Locate every Plasmodium vivax-infected red blood cell.
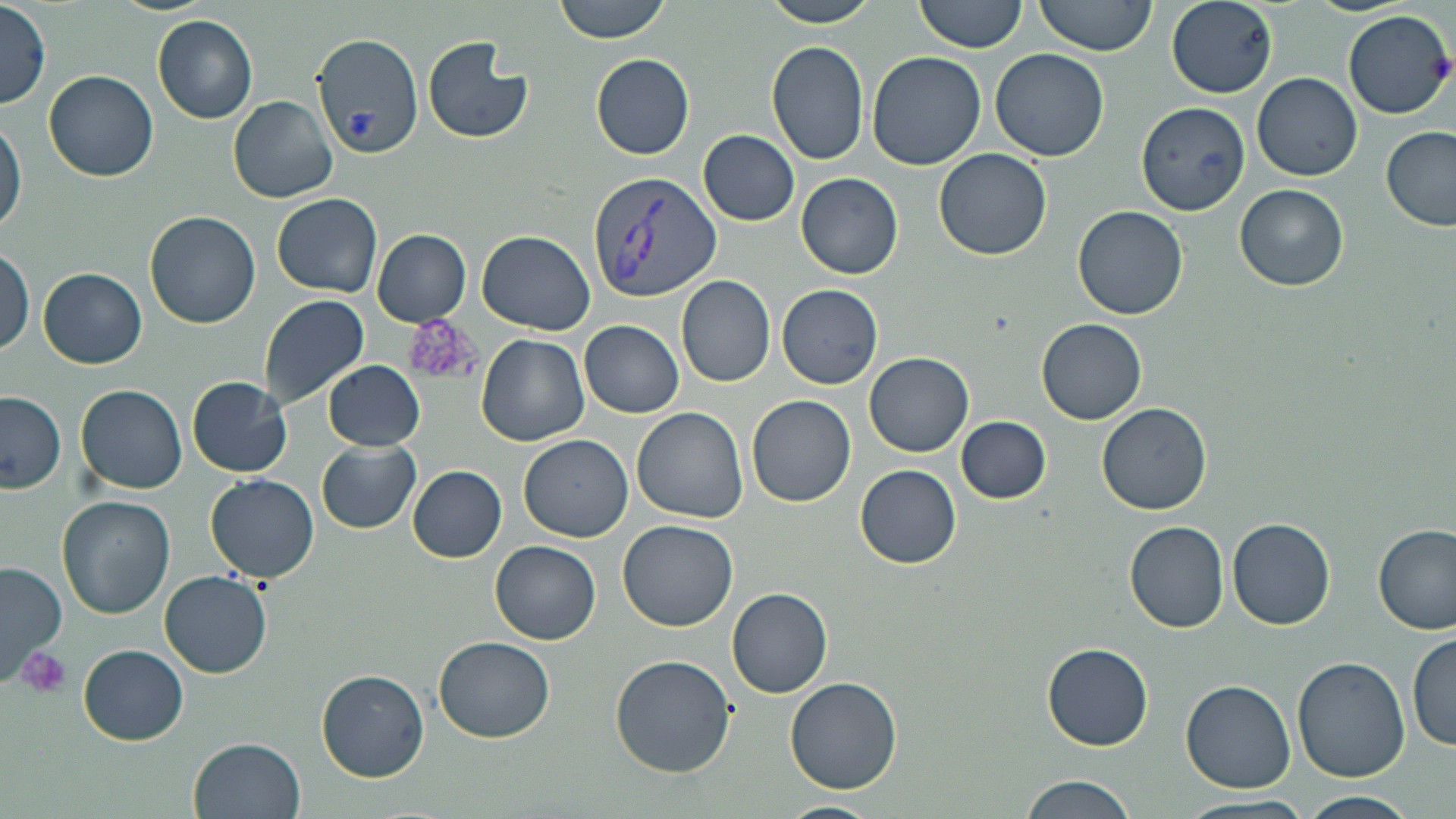

Approximate bounding boxes as [x1, y1, x2, y2] in pixels.
Plasmodium vivax-infected red blood cells: [588, 171, 720, 301].

{
  "slide_level_diagnosis": "Plasmodium vivax",
  "modality": "optical microscopy",
  "image_size": "1456×819 pixels",
  "stain": "May-Grünwald-Giemsa",
  "preparation": "thin blood smear",
  "uninfected_red_blood_cell_locations": "approximate bounding boxes as [x1, y1, x2, y2] in pixels: [552, 0, 672, 43], [759, 0, 881, 26], [914, 0, 1028, 53], [1035, 0, 1157, 55], [1166, 1, 1278, 98], [0, 2, 49, 109], [1343, 9, 1454, 120], [151, 15, 258, 124], [312, 31, 423, 158], [423, 35, 534, 144], [765, 40, 870, 166], [990, 49, 1110, 162], [866, 52, 988, 171], [590, 53, 694, 159], [44, 69, 157, 182], [1251, 72, 1361, 181], [227, 95, 337, 204], [1136, 102, 1252, 216], [1, 116, 28, 235], [1380, 126, 1456, 232], [698, 129, 800, 226], [933, 148, 1053, 260], [795, 173, 903, 279], [1233, 183, 1350, 291], [272, 193, 383, 297], [1071, 205, 1188, 321], [144, 210, 262, 328], [372, 229, 471, 327], [476, 230, 595, 335], [0, 247, 34, 355], [38, 267, 146, 369], [676, 275, 775, 387], [777, 284, 884, 389], [258, 295, 370, 410], [1036, 318, 1149, 424], [578, 321, 683, 417], [476, 334, 589, 446], [863, 352, 974, 458], [322, 361, 425, 450], [186, 376, 292, 478], [75, 385, 188, 495], [0, 392, 65, 492], [746, 394, 856, 507], [1095, 402, 1214, 515], [631, 407, 748, 524], [957, 417, 1052, 503], [519, 435, 633, 541], [316, 440, 421, 534], [320, 457, 502, 553], [854, 464, 961, 567], [408, 466, 507, 563], [205, 474, 319, 583], [57, 496, 176, 620], [1227, 517, 1334, 630], [617, 519, 739, 632], [1124, 522, 1229, 633], [1374, 525, 1456, 635], [490, 541, 602, 643], [0, 560, 69, 681], [158, 570, 272, 677], [726, 588, 834, 698], [734, 622, 857, 769], [1407, 633, 1456, 753], [434, 636, 556, 743], [1041, 642, 1154, 751], [78, 644, 188, 746], [610, 653, 738, 777], [1293, 657, 1409, 783], [317, 669, 429, 781], [784, 675, 905, 794], [1179, 680, 1297, 793], [189, 737, 306, 819], [1019, 775, 1140, 819], [1297, 791, 1423, 818], [1172, 793, 1318, 819], [773, 798, 890, 818]",
  "magnification": "1000x",
  "platelet_locations": "approximate bounding boxes as [x1, y1, x2, y2] in pixels: [401, 318, 484, 390], [20, 647, 73, 694]",
  "field_of_view": "single"
}